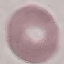

malaria status = uninfected
capture = smartphone camera at the microscope eyepiece
preparation = thin blood smear
image type = automatically extracted cell patch, resized to 64 × 64 pixels
stain = Giemsa